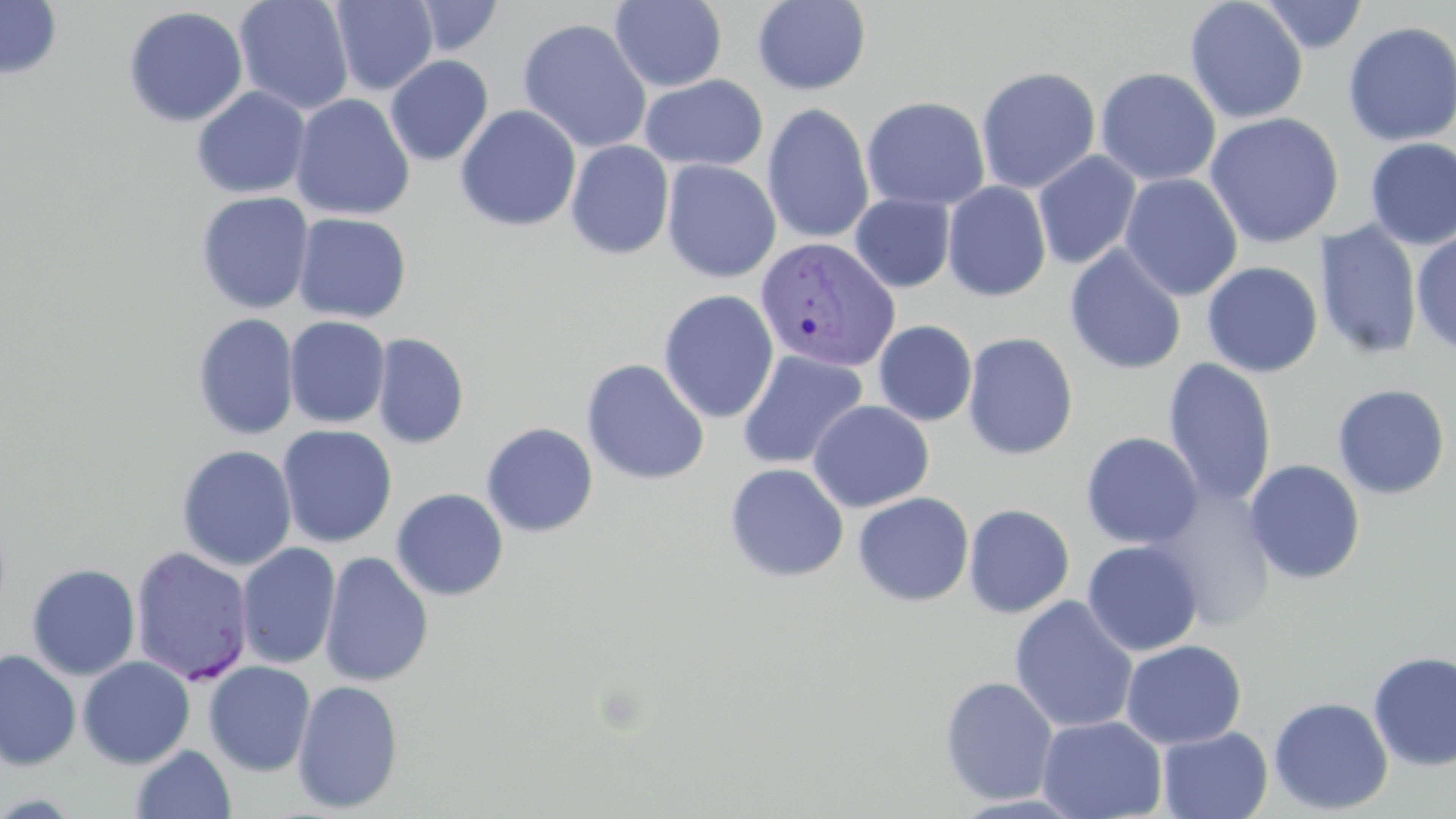

Summary:
  - Coordinate format: approximate bounding boxes as (x1, y1, x2, y2) in pixels
  - Plasmodium vivax-infected red blood cell locations: (755, 235, 901, 373), (129, 545, 254, 686)
  - Uninfected red blood cell locations: (0, 0, 63, 81), (233, 0, 354, 115), (411, 0, 504, 56), (609, 0, 727, 92), (751, 0, 872, 95), (1258, 0, 1368, 54), (330, 1, 438, 95), (1184, 1, 1308, 124), (122, 6, 248, 127), (517, 18, 652, 154), (1342, 20, 1456, 147), (385, 55, 494, 166), (975, 65, 1101, 194), (1095, 67, 1221, 187), (639, 75, 769, 172), (191, 86, 311, 199), (290, 93, 415, 221), (861, 96, 991, 211), (761, 103, 875, 244), (455, 104, 581, 231), (1204, 111, 1344, 249), (1363, 137, 1456, 249), (566, 140, 674, 260), (1033, 150, 1141, 269), (662, 160, 781, 282), (1119, 173, 1243, 302), (942, 180, 1052, 302), (195, 191, 315, 315), (850, 193, 955, 292), (292, 212, 412, 324), (1314, 222, 1423, 360), (1411, 229, 1456, 356), (1064, 244, 1187, 375), (1201, 261, 1323, 378), (658, 289, 779, 424), (192, 313, 299, 440), (284, 316, 391, 429), (873, 320, 978, 426), (371, 332, 470, 450), (962, 332, 1079, 460), (737, 350, 868, 471), (581, 358, 709, 486), (1163, 358, 1277, 507), (1331, 383, 1451, 500), (807, 400, 935, 513), (481, 422, 599, 537), (277, 425, 398, 547), (1081, 432, 1203, 549), (175, 444, 297, 571), (1244, 459, 1366, 585), (723, 463, 849, 582), (1147, 485, 1277, 632), (391, 488, 509, 601), (853, 492, 974, 607), (963, 504, 1075, 618), (1082, 539, 1203, 656), (223, 540, 326, 773), (236, 542, 341, 670), (319, 551, 434, 687), (26, 563, 141, 680), (1009, 595, 1139, 734), (1121, 639, 1247, 749), (0, 649, 82, 771), (1367, 650, 1456, 772), (77, 656, 195, 769), (203, 661, 316, 776), (939, 676, 1059, 805), (292, 679, 405, 814), (1268, 696, 1393, 815), (1037, 715, 1167, 819), (1157, 726, 1273, 818), (131, 745, 236, 819)
  - Slide-level diagnosis: Plasmodium vivax
  - Field of view: single
  - Image size: 1456×819 pixels
  - Preparation: thin blood film
  - Stain: May-Grünwald-Giemsa
  - Magnification: 1000x
  - Modality: light microscopy